Report the malaria status of this cell.
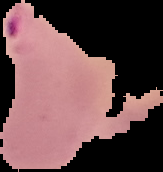

Parasitized.

image_size: 163×172 pixels
image_type: cell region segmented out of the field of view; surrounding area masked to black
preparation: thin blood smear